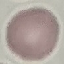
Summary:
  - Result: no malaria parasites seen
  - Stain: Giemsa
  - Preparation: thin blood film
  - Capture: smartphone through the microscope eyepiece
  - Image type: cell patch, automatically extracted from a larger field of view and resized to 64 × 64 pixels